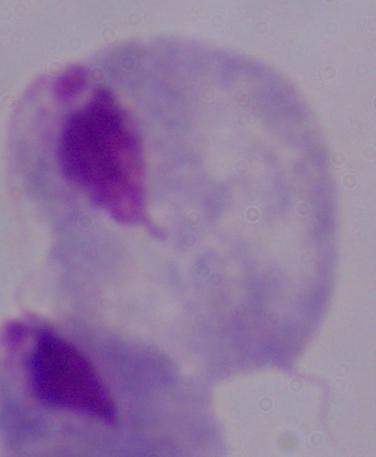
A trichomonad is seen. Photomicrograph. 1000x magnification.